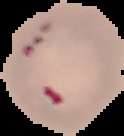
image type = segmented cell region on a black background
preparation = thin blood smear
malaria status = parasitized
image size = 124×136 pixels